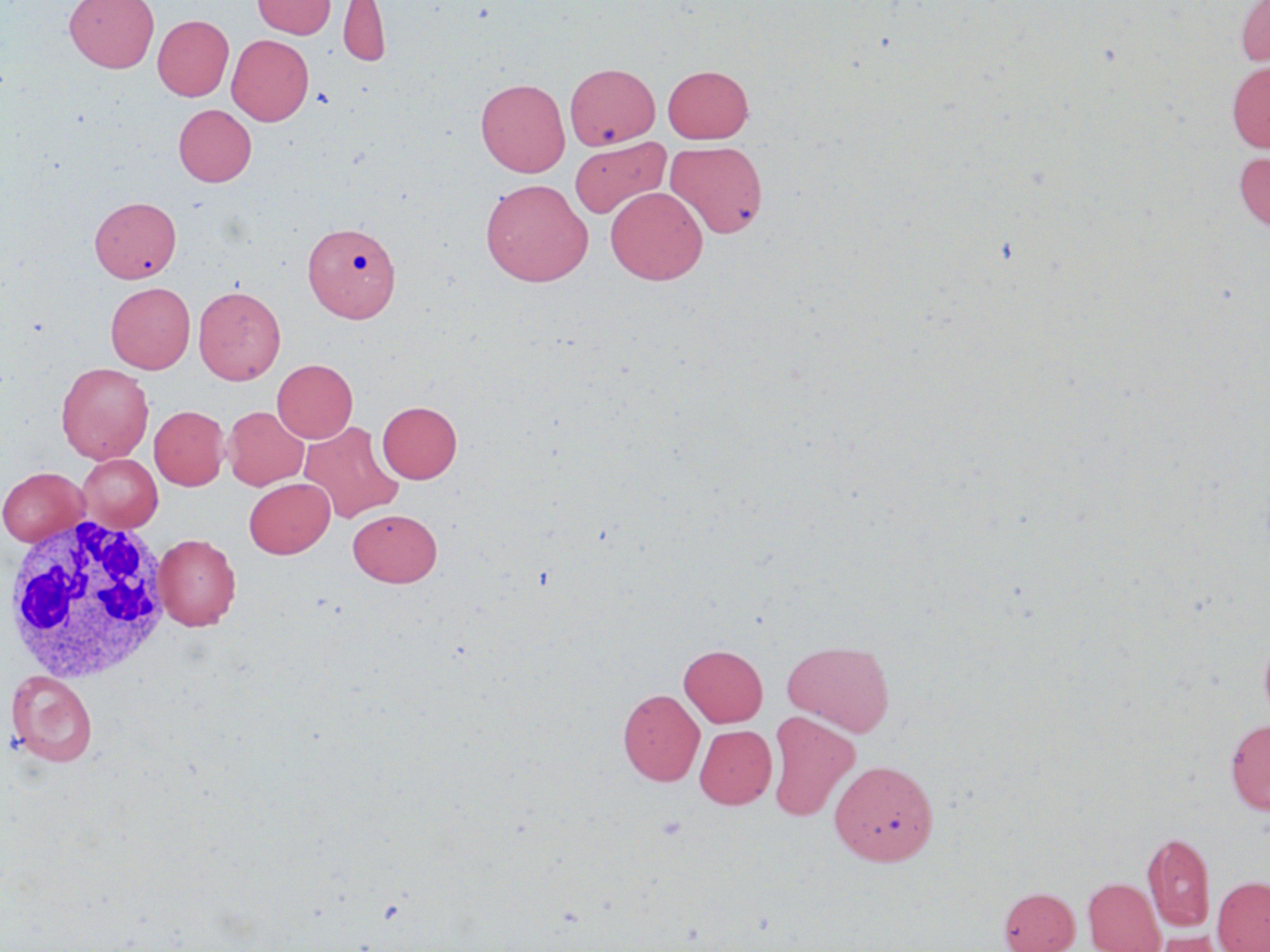 Approximate bounding boxes as (x1, y1, x2, y2) in pixels. White blood cell locations: (2, 512, 173, 686). Uninfected red blood cell locations: (65, 0, 159, 72), (251, 0, 336, 38), (338, 0, 390, 69), (1235, 0, 1270, 66), (153, 15, 233, 101), (227, 34, 314, 125), (1227, 61, 1270, 152), (566, 62, 660, 149), (662, 65, 753, 143), (475, 78, 570, 176), (173, 104, 256, 186), (569, 139, 671, 221), (665, 140, 768, 239), (1233, 150, 1270, 231), (480, 178, 593, 286), (605, 186, 708, 285), (90, 196, 181, 283), (304, 222, 401, 322), (106, 282, 195, 373), (194, 285, 285, 384), (272, 359, 357, 443), (56, 362, 154, 464), (377, 401, 462, 483), (149, 406, 229, 490), (223, 406, 308, 490), (299, 420, 404, 524), (78, 454, 162, 532), (1, 467, 90, 546), (244, 478, 334, 558), (347, 509, 442, 586), (153, 533, 240, 630), (1260, 630, 1270, 730), (782, 639, 895, 736), (679, 644, 767, 727), (6, 670, 98, 766), (618, 689, 705, 785), (766, 711, 860, 822), (1225, 719, 1270, 815), (695, 725, 776, 809), (830, 759, 939, 866), (1142, 832, 1215, 931), (1212, 876, 1270, 952), (1083, 877, 1164, 951), (999, 886, 1079, 952), (1143, 930, 1229, 952). Slide-level diagnosis: no evidence of blood parasites. One field of a larger specimen. May-Grünwald-Giemsa stain. 1000x magnification. Thin blood film. Optical microscopy. Image is 1270×952 pixels.